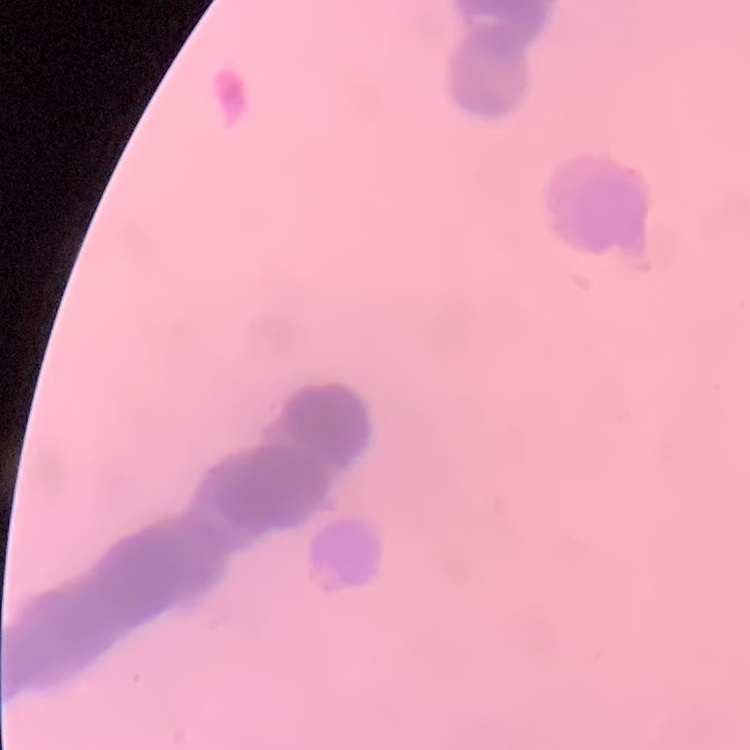
red blood cell morphology = rouleaux formation
preparation = thin blood film
stain = Field's or Giemsa
image type = square crop of a larger photomicrograph